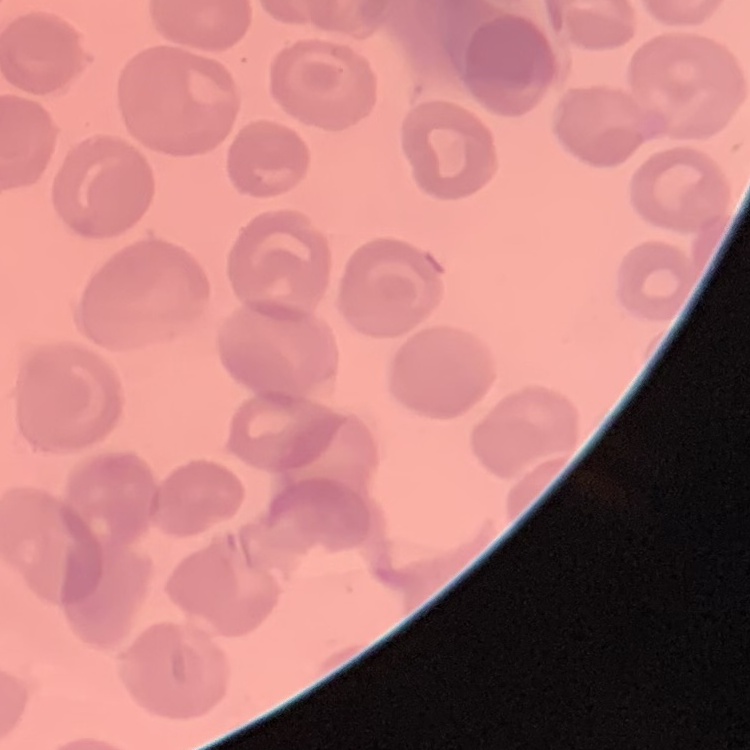
erythrocyte_morphology: no rouleaux formation
image_type: one tile cut from a larger photomicrograph
preparation: thin peripheral smear
stain: Field's or Giemsa